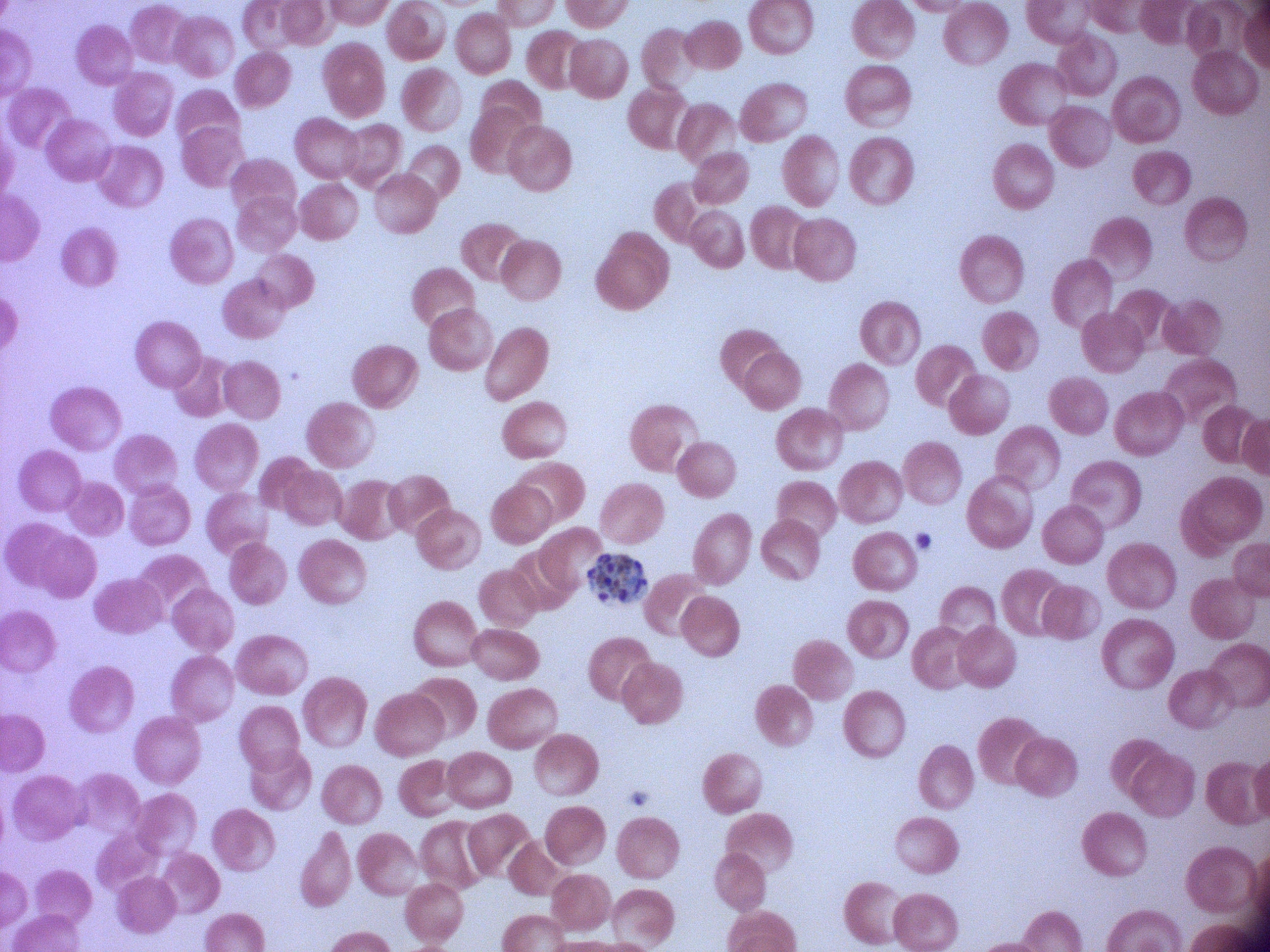

Approximate bounding boxes as named x1/y1/x2/y2 corners in pixels, from the source annotation, which is not necessarily exhaustive.
Summary:
  - Schizont locations: (x1=587, y1=553, x2=647, y2=603)
  - Stain: Giemsa
  - Magnification: 100x
  - Species: Plasmodium falciparum
  - Preparation: thin blood smear
  - Image size: 1270×952 pixels
  - Field of view: one from this slide
  - Microscope: Leica DM2000 with built-in camera